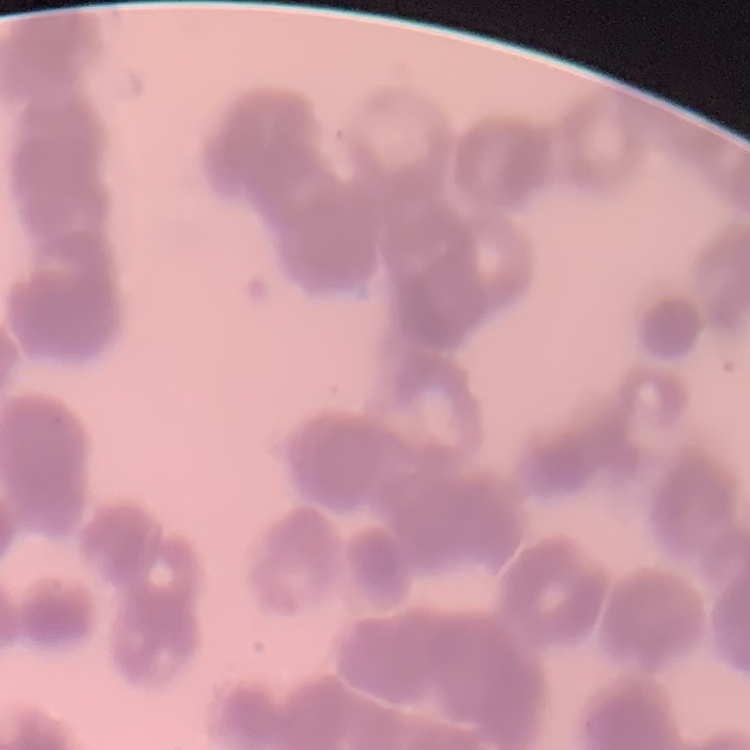
The erythrocytes show rouleaux formation. One tile cut from a larger photomicrograph. Stained with either Field's or Giemsa. Thin blood film.